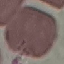
Summary:
  - Result: negative for malaria parasites
  - Preparation: thin blood smear
  - Capture: smartphone through the microscope eyepiece
  - Stain: Giemsa
  - Image type: automatically extracted cell patch, resized to 64 × 64 pixels